Describe the morphology of the erythrocytes.
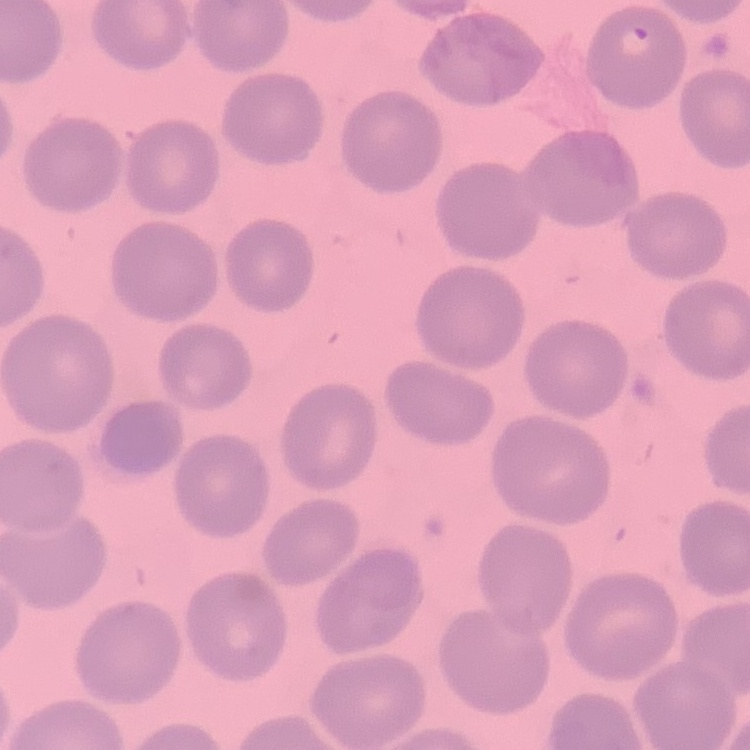
They show no rouleaux formation.

Summary:
  - Preparation: thin blood film
  - Image type: square crop of a larger photomicrograph
  - Stain: Field's or Giemsa